Give the extent of all uninfected red blood cells.
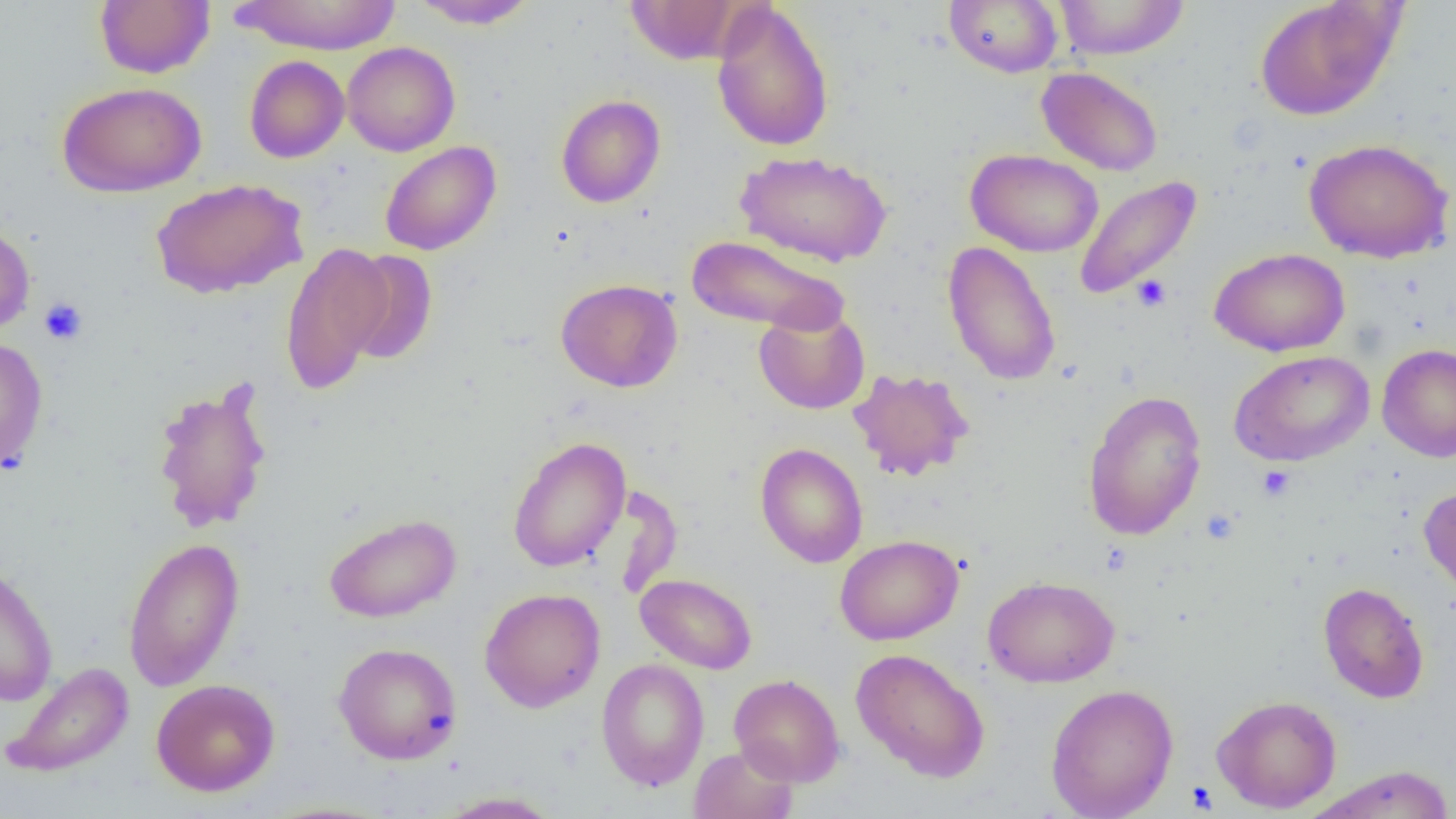
Approximate bounding boxes as (x1,y1)-(x2,y2) corner pairs in pixels.
Uninfected red blood cells: (94,0)-(215,79), (230,0)-(402,55), (409,0)-(539,30), (944,0)-(1063,78), (1054,0)-(1190,60), (1254,0)-(1402,122), (625,1)-(742,64), (711,1)-(835,152), (342,42)-(460,157), (244,55)-(350,163), (1036,66)-(1163,177), (56,81)-(207,197), (555,94)-(666,208), (1303,137)-(1454,263), (379,141)-(501,256), (965,148)-(1104,257), (735,150)-(892,267), (1073,175)-(1202,301), (150,177)-(309,299), (0,221)-(35,336), (687,234)-(849,335), (943,241)-(1062,387), (279,242)-(394,394), (1209,247)-(1350,357), (341,249)-(439,365), (555,278)-(683,392), (753,306)-(870,415), (0,335)-(48,472), (1376,344)-(1456,462), (1229,350)-(1374,467), (847,367)-(976,481), (151,379)-(274,534), (1083,389)-(1208,541), (507,436)-(631,572), (754,443)-(868,568), (1418,485)-(1456,604), (323,512)-(462,623), (835,535)-(963,645), (122,536)-(245,692), (0,561)-(59,706), (635,573)-(758,674), (982,575)-(1120,688), (1318,581)-(1429,703), (479,588)-(606,712), (333,642)-(462,764), (850,647)-(991,783), (596,659)-(710,791), (1,660)-(134,778), (729,673)-(845,787), (151,678)-(280,797), (1045,683)-(1179,819), (1211,694)-(1342,813), (689,744)-(798,819), (1306,766)-(1456,819), (435,791)-(564,818).

{
  "slide_level_diagnosis": "no evidence of blood parasites",
  "image_size": "1456×819 pixels",
  "magnification": "1000x",
  "modality": "light microscopy",
  "field_of_view": "one of a larger specimen",
  "platelet_locations": "approximate bounding boxes as (x1,y1)-(x2,y2) corner pairs in pixels: (1132,274)-(1172,312), (39,297)-(88,345), (1257,465)-(1295,501)",
  "preparation": "thin blood smear"
}